Name the parasite shown.
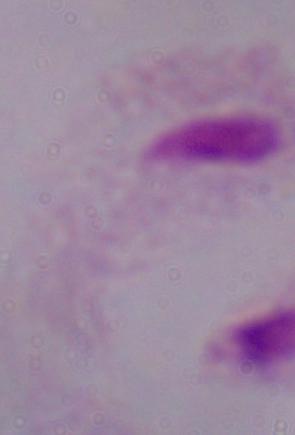

This is a trichomonad.

1000x magnification. Photomicrograph.